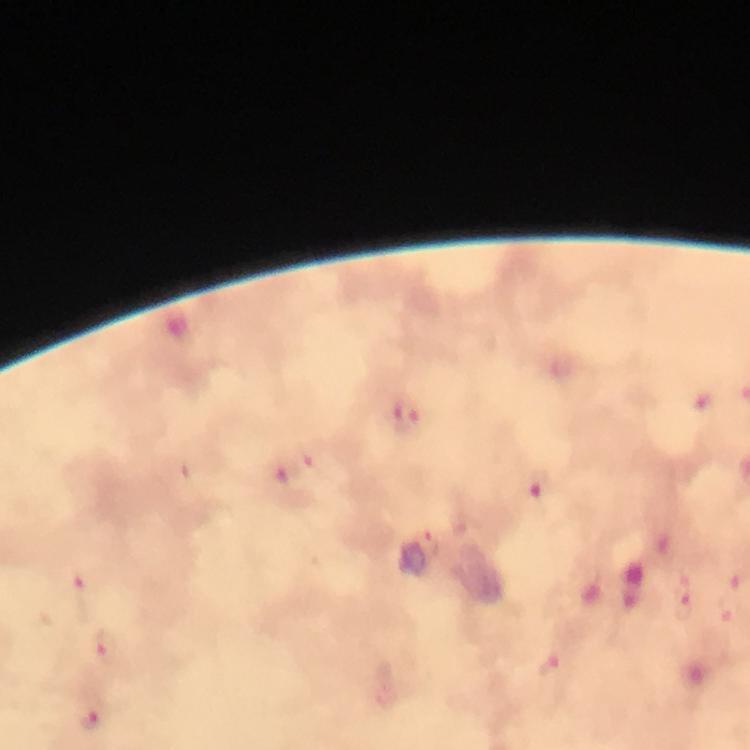

immersion_oil: applied
cropped_from: one field of view
stain: Giemsa
preparation: thick smear
malaria_parasite_locations: 'approximate centers as (x, y) in pixels: (405, 413), (540, 485), (430, 543), (81, 585), (684, 606), (729, 612), (105, 645), (548, 666), (92, 719)'
context: from a diagnostic examination for malaria
capture: smartphone photograph through a microscope
magnification: 100x
image_size: 750×750 pixels